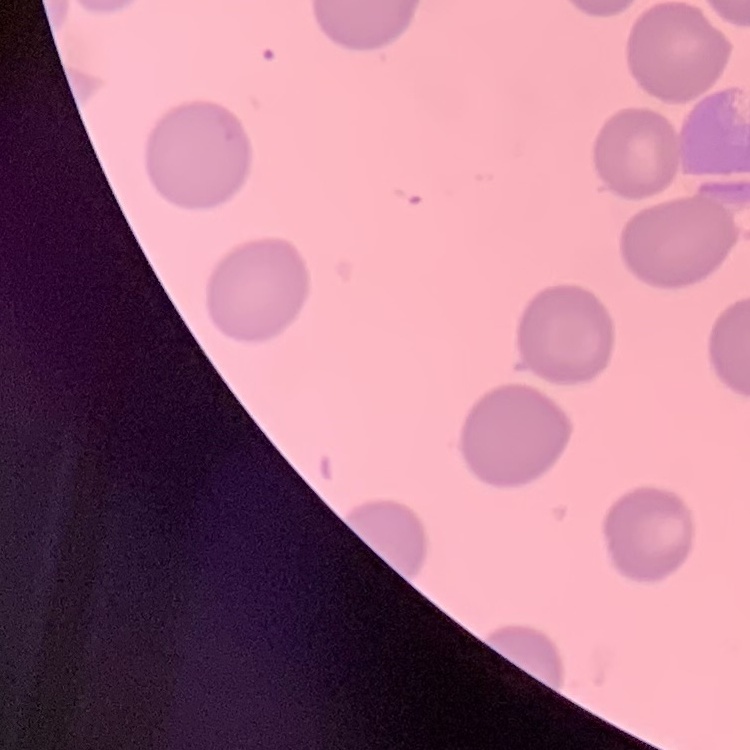
The red blood cells exhibit no rouleaux formation. Square crop of a larger photomicrograph. Thin blood smear. Stained with either Field's or Giemsa.